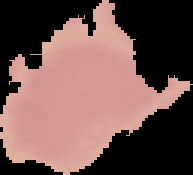
From a thin blood film. Cell region segmented out of the field of view; the surrounding area is masked to black. Image is 193×175 pixels. Result: no malaria parasites detected.